Assess this cell for malaria.
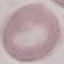

Uninfected.

Summary:
  - Image type: automatically extracted cell patch, resized to 64 × 64 pixels
  - Capture: smartphone camera at the microscope eyepiece
  - Stain: Giemsa
  - Preparation: thin blood smear